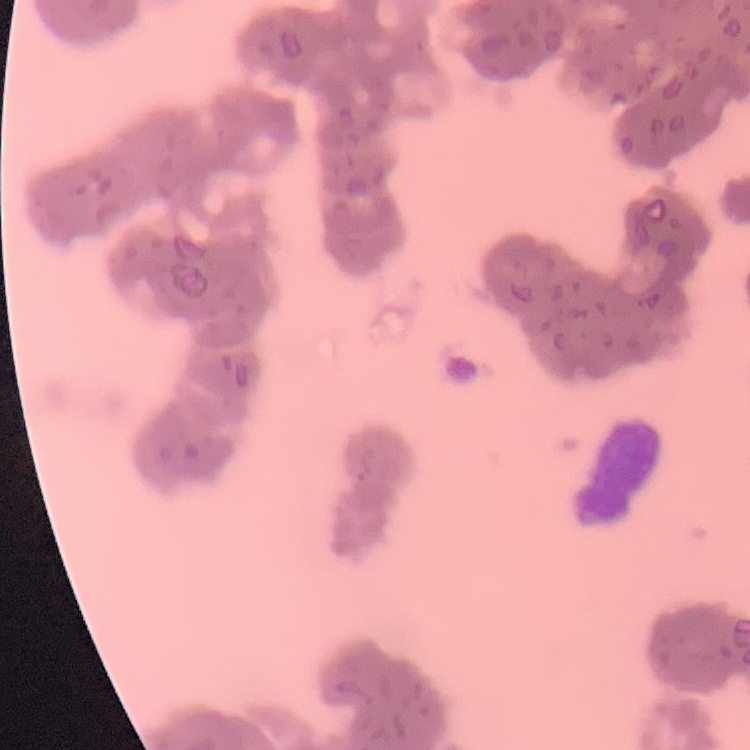

Summary:
  - Erythrocyte morphology: rouleaux formation
  - Stain: Field's or Giemsa
  - Image type: one tile cut from a larger photomicrograph
  - Preparation: thin blood film